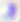

{
  "magnification": "400x",
  "modality": "micrograph",
  "identification": "Toxoplasma gondii"
}